Evaluate for Plasmodium parasites.
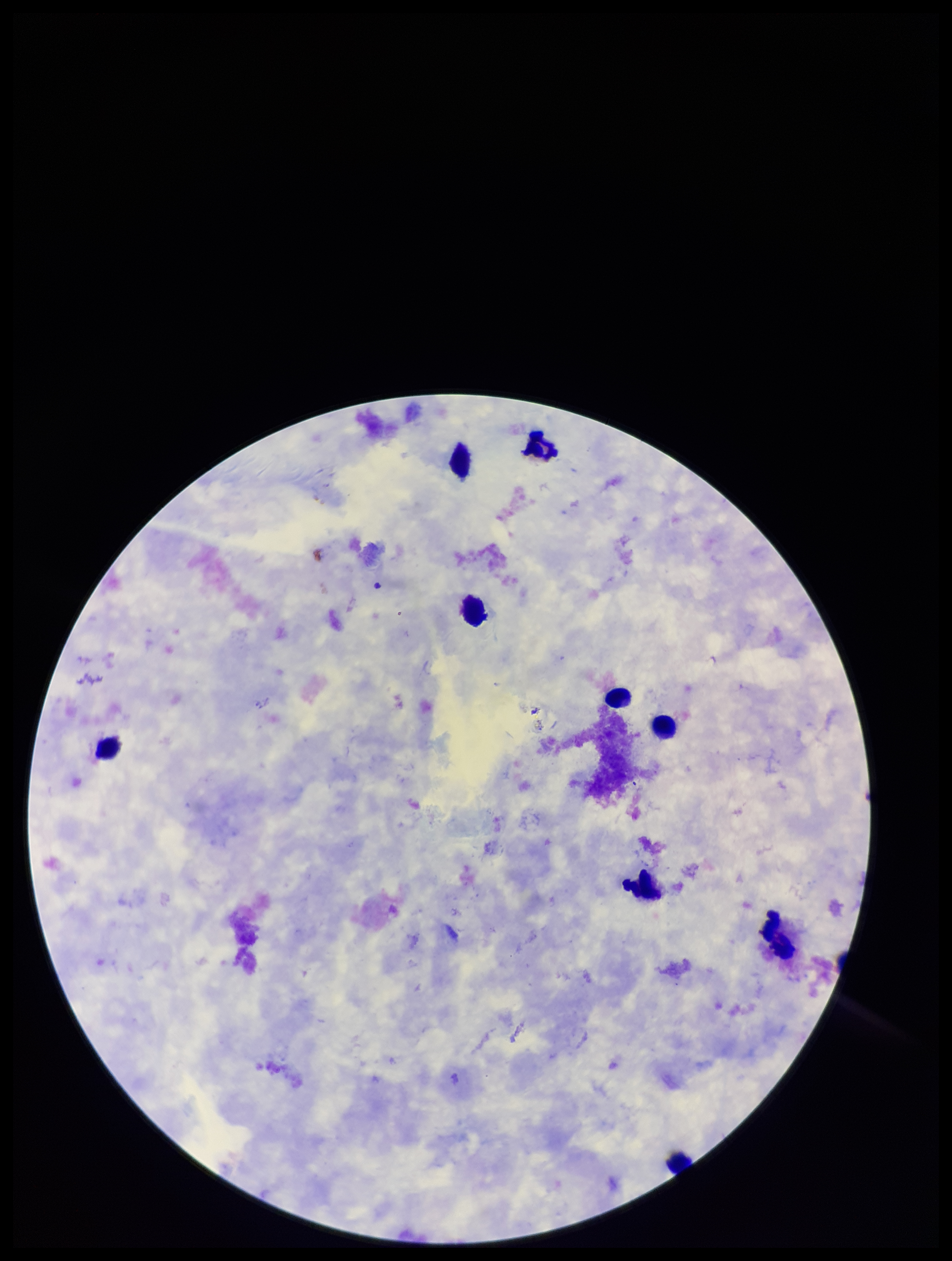
None identified.

Photographed through the microscope eyepiece with a smartphone camera. Image is 952×1261 pixels. Patient malaria status: negative. Single field of view. Parasite count: 0. Preparation: thick blood smear. Leukocyte count: 9. Stained with Giemsa.